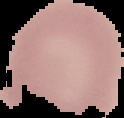

Summary:
  - Image size: 124×118 pixels
  - Preparation: thin blood smear
  - Result: no malaria parasites detected
  - Image type: segmented cell region on a black background